Rate the background quality.
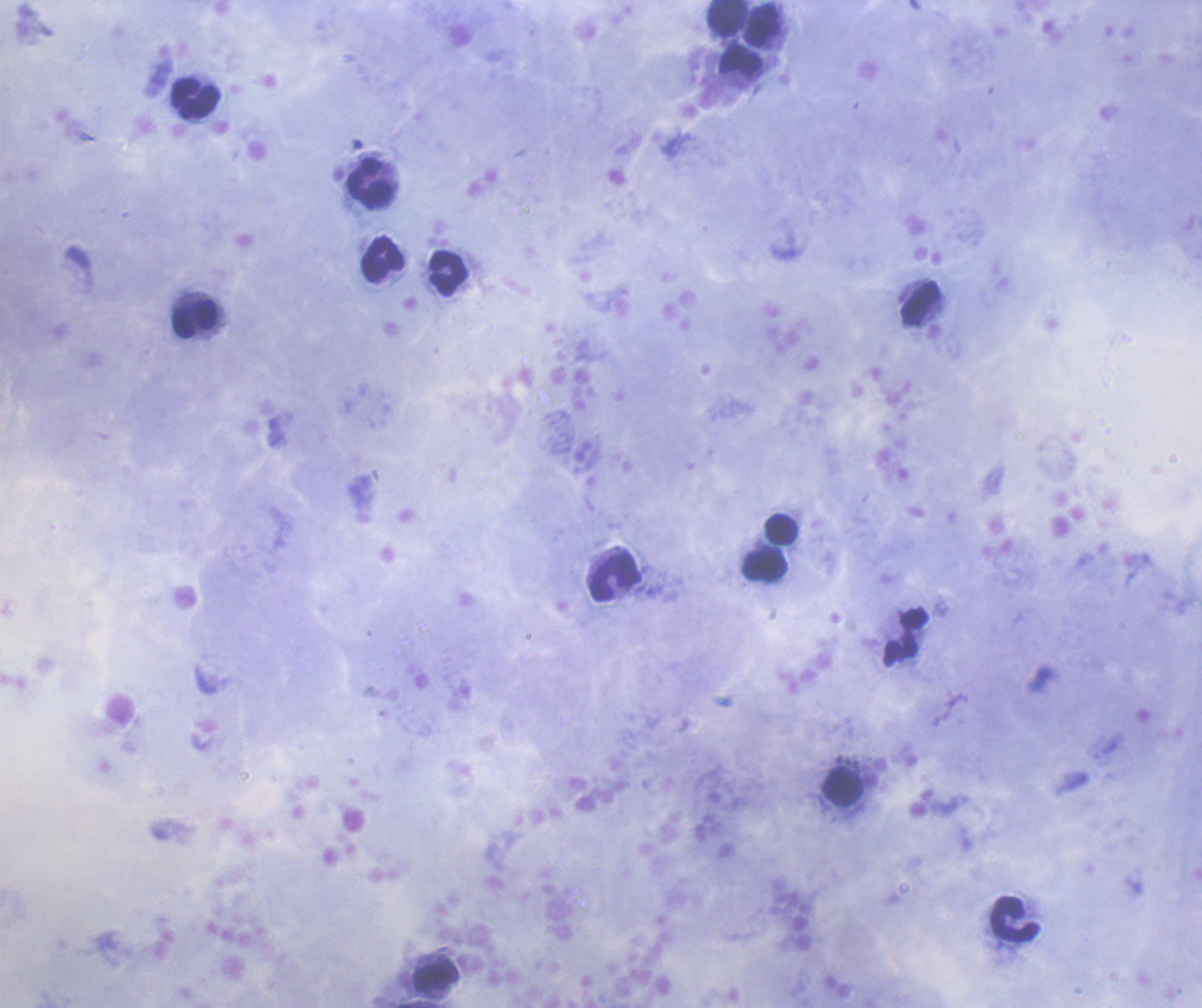
Good.

Approximate object centers, in pixels from the top-left corner. Leukocyte locations: (x=728, y=18), (x=763, y=25), (x=741, y=60), (x=196, y=99), (x=371, y=184), (x=382, y=259), (x=450, y=273), (x=918, y=303), (x=194, y=318), (x=781, y=528), (x=765, y=562), (x=615, y=577), (x=906, y=637), (x=841, y=787), (x=1014, y=920), (x=436, y=976). Previously used in a real diagnosis. Thick blood film. Coloration quality: good. Result: negative for malaria parasites. Single field of view. Romanowsky-stained preparation. 100x magnification. Image is 1202×1008 pixels.